Locate every Plasmodium parasite.
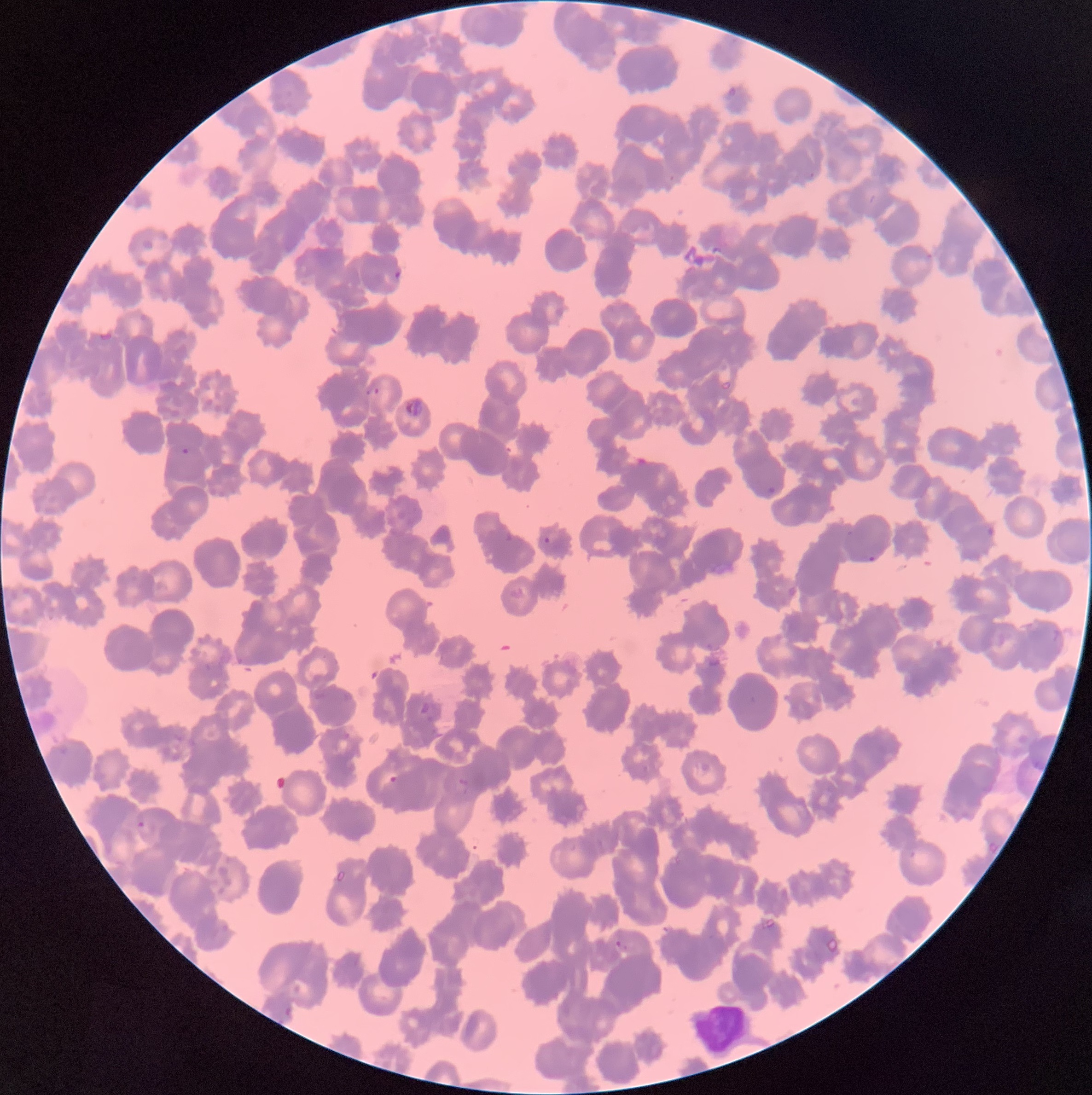
Approximate bounding boxes as (x1,y1)-(x2,y2) corner pairs in pixels.
Plasmodium parasites: (727,86)-(737,98), (868,194)-(876,204), (923,249)-(934,261), (391,269)-(402,282), (138,312)-(150,324), (366,387)-(382,399), (402,397)-(423,418), (181,447)-(190,455), (765,487)-(777,495), (866,555)-(876,561), (1051,624)-(1065,649), (745,696)-(758,707), (388,776)-(398,785), (455,778)-(468,796), (137,818)-(157,841), (899,848)-(916,863), (615,940)-(628,952).
Plasmodium parasites too small for a box (approximate centers as (x,y) in pixels): (812,175), (671,178), (849,533), (546,540).

Summary:
  - White blood cell locations: (687,1007)-(754,1055)
  - Preparation: thin blood smear
  - Red blood cell morphology: rouleaux formation
  - Modality: optical microscopy
  - Image size: 1092×1095 pixels